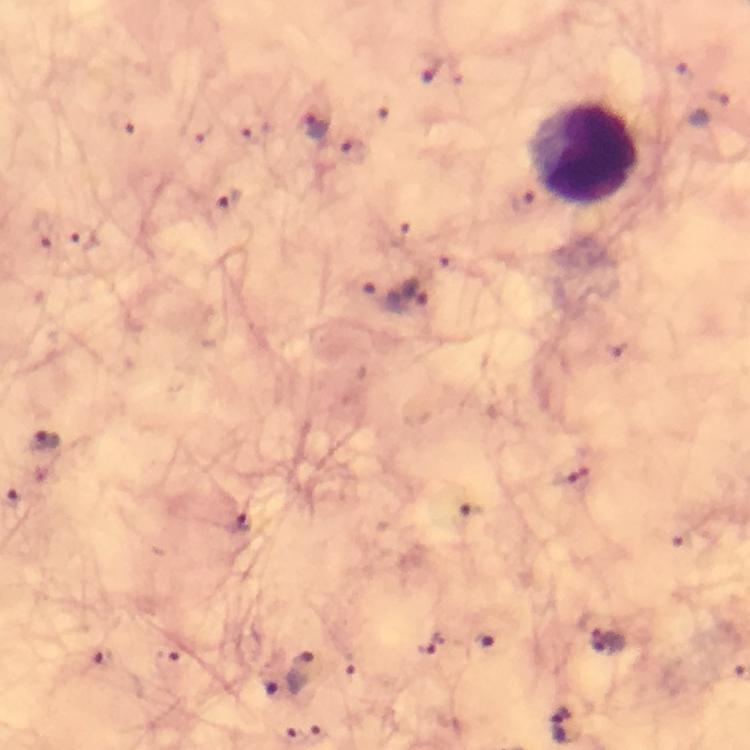
{
  "leukocyte_locations": "approximate object centers, in pixels from the top-left corner: (x=583, y=154)",
  "capture": "smartphone photograph through a microscope",
  "plasmodium_parasite_locations": "approximate object centers, in pixels from the top-left corner: (x=427, y=68), (x=710, y=111), (x=122, y=125), (x=253, y=127), (x=316, y=127), (x=350, y=151), (x=228, y=208), (x=43, y=231), (x=398, y=236), (x=81, y=238), (x=418, y=290), (x=381, y=294), (x=42, y=443), (x=569, y=473), (x=470, y=515), (x=239, y=522), (x=590, y=624), (x=484, y=638), (x=430, y=644), (x=607, y=644), (x=166, y=657), (x=103, y=659), (x=346, y=663), (x=303, y=677), (x=267, y=689), (x=562, y=726), (x=314, y=735), (x=287, y=736)",
  "stain": "Giemsa",
  "preparation": "thick blood film",
  "image_size": "750×750 pixels",
  "magnification": "100x",
  "immersion_oil": "used",
  "cropped_from": "one field of view",
  "context": "from a diagnostic examination for malaria"
}